Identify the cell.
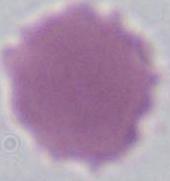

An erythrocyte.

Summary:
  - Modality: micrograph
  - Magnification: 1000x